Locate and identify every blood parasite.
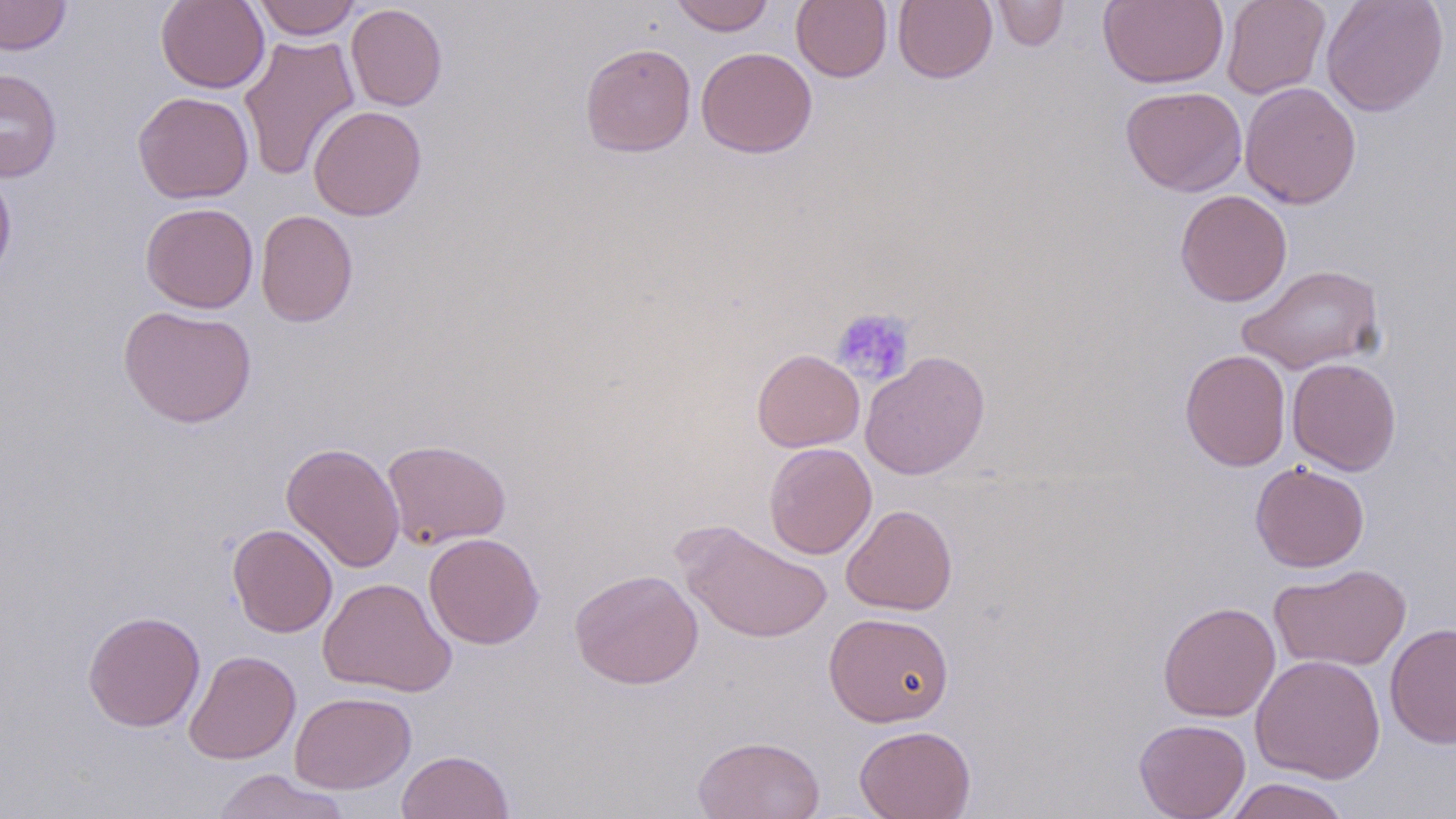

No blood parasites seen.

Summary:
  - Coordinate format: approximate bounding boxes as (x1, y1, x2, y2) in pixels
  - Platelet locations: (832, 307, 916, 386)
  - Uninfected red blood cell locations: (0, 0, 71, 54), (156, 0, 269, 93), (251, 0, 362, 40), (669, 0, 775, 35), (791, 0, 892, 82), (893, 0, 997, 84), (990, 0, 1069, 51), (1098, 0, 1229, 89), (1221, 0, 1330, 100), (1321, 0, 1448, 116), (346, 4, 448, 111), (238, 33, 361, 181), (579, 42, 697, 157), (696, 46, 818, 158), (0, 68, 62, 182), (1239, 82, 1362, 209), (1121, 85, 1247, 197), (132, 91, 254, 204), (308, 104, 427, 221), (0, 168, 17, 286), (1174, 190, 1292, 306), (140, 202, 259, 313), (256, 210, 358, 327), (1236, 264, 1386, 375), (118, 304, 257, 428), (752, 348, 865, 452), (1180, 349, 1292, 471), (860, 350, 990, 480), (1287, 357, 1401, 475), (381, 439, 511, 550), (280, 441, 405, 573), (764, 442, 877, 559), (1250, 462, 1370, 572), (841, 504, 958, 615), (675, 520, 833, 644), (227, 523, 338, 638), (424, 532, 544, 649), (1268, 564, 1412, 671), (569, 568, 704, 688), (317, 577, 456, 697), (1157, 601, 1281, 722), (82, 610, 205, 732), (824, 611, 955, 727), (1385, 623, 1456, 748), (184, 650, 301, 765), (1250, 654, 1385, 784), (289, 690, 416, 794), (1134, 718, 1250, 819), (854, 724, 976, 819), (693, 735, 825, 819), (396, 749, 515, 819), (210, 768, 352, 819), (1223, 778, 1352, 819)
  - Slide-level diagnosis: negative for blood parasites
  - Magnification: 1000x
  - Stain: May-Grünwald-Giemsa
  - Image size: 1456×819 pixels
  - Field of view: single
  - Preparation: thin blood film
  - Modality: optical microscopy